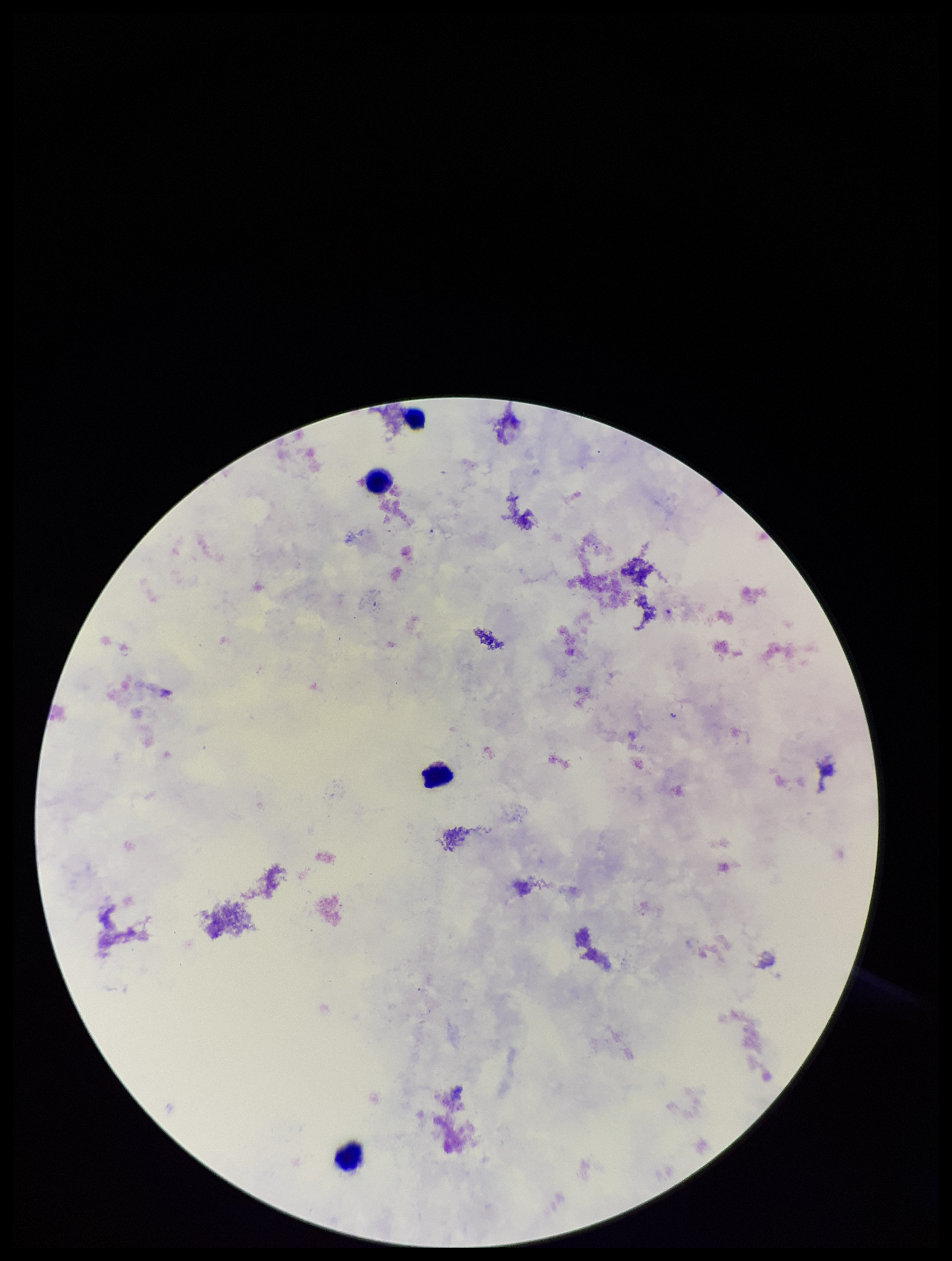

field of view = single
preparation = thick
Plasmodium parasites = none detected
capture = smartphone photograph through the microscope eyepiece
leukocyte count = 4
image size = 952×1261 pixels
stain = Giemsa
patient malaria status = negative
parasite count = 0